Name the parasite shown.
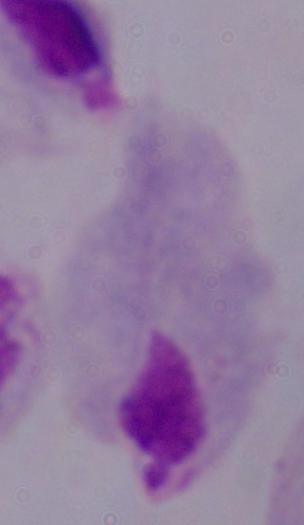
This is a trichomonad.

Micrograph. 1000x magnification.